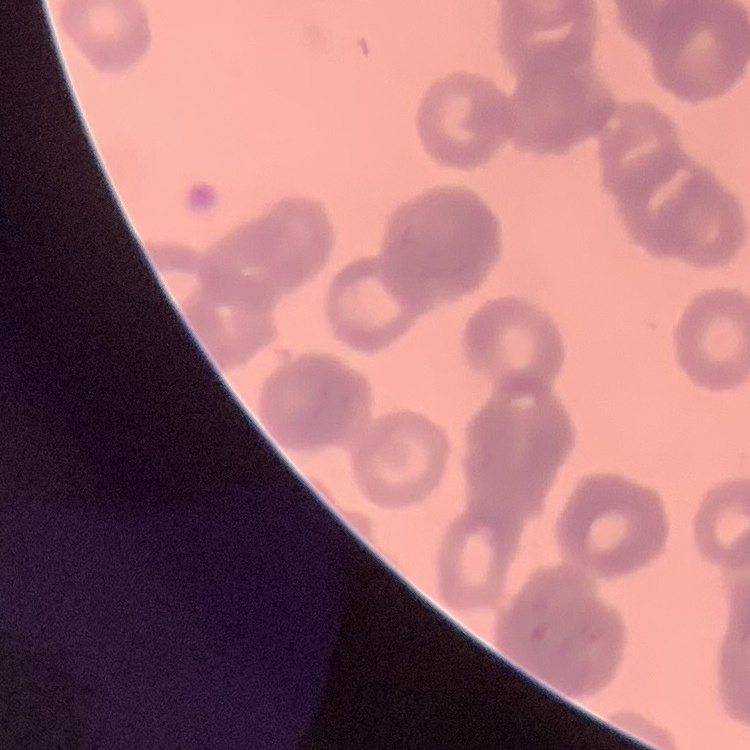 The red blood cells exhibit rouleaux formation. Stained with either Field's or Giemsa. Thin peripheral smear. One tile cut from a larger photomicrograph.